Report the malaria status of this cell.
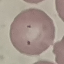
Parasitized.

Summary:
  - Stain: Giemsa
  - Preparation: thin blood smear
  - Image type: automatically extracted cell patch, resized to 64 × 64 pixels
  - Capture: smartphone camera at the microscope eyepiece